Report the malaria status of this cell.
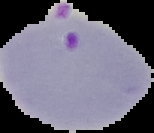
Parasitized.

Summary:
  - Preparation: thin blood film
  - Image type: segmented cell region with the area outside set to black
  - Image size: 154×133 pixels